Point out malaria parasites and leukocytes.
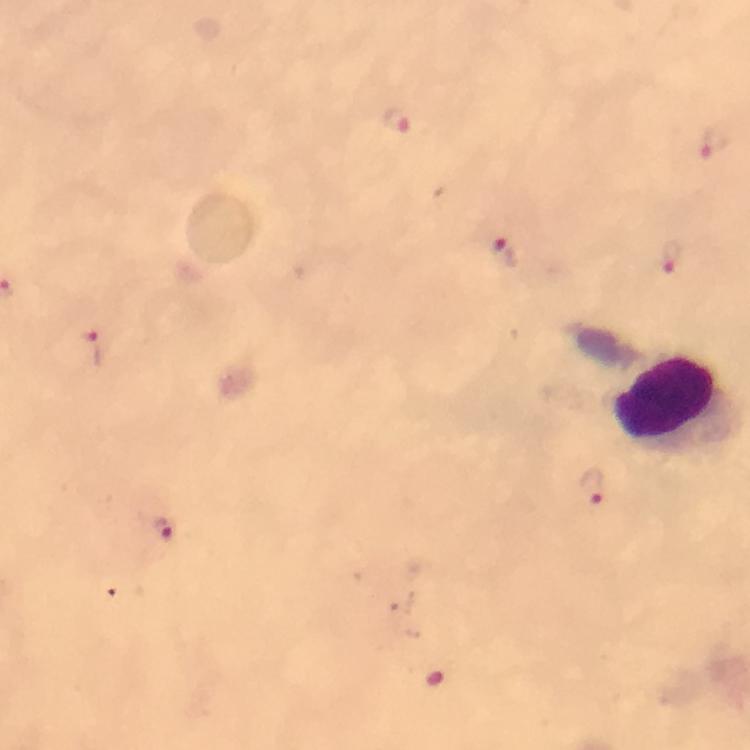

Approximate centers as (x, y) in pixels.
Malaria parasites: (396, 118), (717, 142), (505, 253), (671, 257), (95, 347), (591, 483), (163, 528).
Leukocytes: (667, 397).

A crop from one field of view. 100x magnification. Smartphone photograph taken through a microscope. Image is 750×750 pixels. Giemsa-stained preparation. Thick blood film. Immersion oil was used. From a diagnostic examination for malaria.